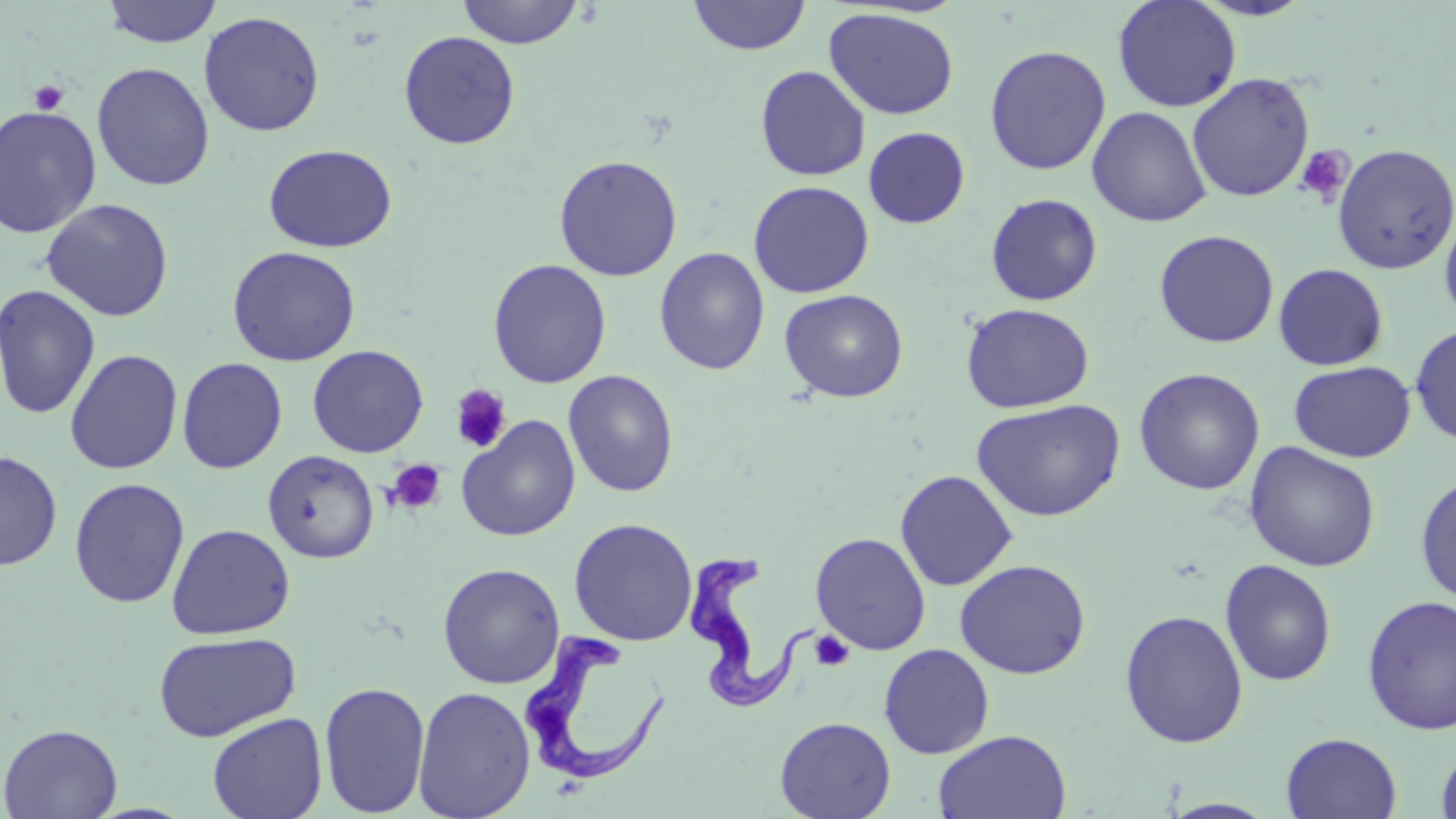
Summary:
  - Coordinate format: approximate bounding boxes as (x1,y1)-(x2,y2) corner pairs in pixels
  - Platelet locations: (28,79)-(69,115), (1294,145)-(1353,206), (450,384)-(512,453), (385,459)-(447,516), (809,630)-(855,672)
  - Trypanosoma brucei locations: (684,552)-(819,717), (522,628)-(671,789)
  - Uninfected red blood cell locations: (101,0)-(222,48), (456,0)-(585,49), (688,0)-(811,55), (1112,0)-(1242,113), (1194,0)-(1314,21), (823,7)-(960,120), (198,11)-(325,137), (399,30)-(521,149), (984,44)-(1111,175), (91,62)-(216,192), (755,65)-(871,181), (1187,72)-(1315,203), (0,104)-(102,238), (1087,106)-(1212,227), (863,126)-(971,229), (262,143)-(397,253), (1332,143)-(1455,275), (553,154)-(683,282), (748,180)-(875,298), (985,192)-(1103,306), (40,198)-(174,322), (1439,206)-(1456,331), (1153,229)-(1279,348), (226,246)-(361,367), (654,247)-(770,376), (487,259)-(612,389), (1273,263)-(1389,370), (0,283)-(102,420), (779,288)-(908,403), (960,303)-(1095,413), (1410,324)-(1456,446), (307,344)-(429,457), (64,349)-(183,475), (176,357)-(288,474), (1289,361)-(1416,463), (1133,367)-(1266,495), (563,370)-(679,498), (971,398)-(1126,522), (457,416)-(581,541), (1244,441)-(1381,572), (0,449)-(62,570), (263,449)-(379,563), (895,469)-(1018,591), (1414,471)-(1456,606), (68,477)-(191,608), (568,517)-(698,646), (166,523)-(296,639), (810,532)-(931,655), (954,558)-(1091,679), (1220,559)-(1338,687), (438,563)-(565,689), (1361,595)-(1456,736), (1119,609)-(1249,749), (152,631)-(301,743), (879,643)-(994,759), (318,680)-(431,817), (412,686)-(536,819), (207,712)-(328,819), (774,716)-(896,819), (1,722)-(123,818), (933,729)-(1072,819), (1281,732)-(1402,818), (1436,741)-(1456,819), (1158,798)-(1282,818)
  - Slide-level diagnosis: Trypanosoma brucei
  - Stain: May-Grünwald-Giemsa
  - Field of view: one of a larger specimen
  - Magnification: 1000x
  - Image size: 1456×819 pixels
  - Modality: optical microscopy
  - Preparation: thin blood film